Name the parasite shown.
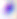

This is Toxoplasma gondii.

Photomicrograph. Captured at 400x magnification.